Identify the blood parasite species.
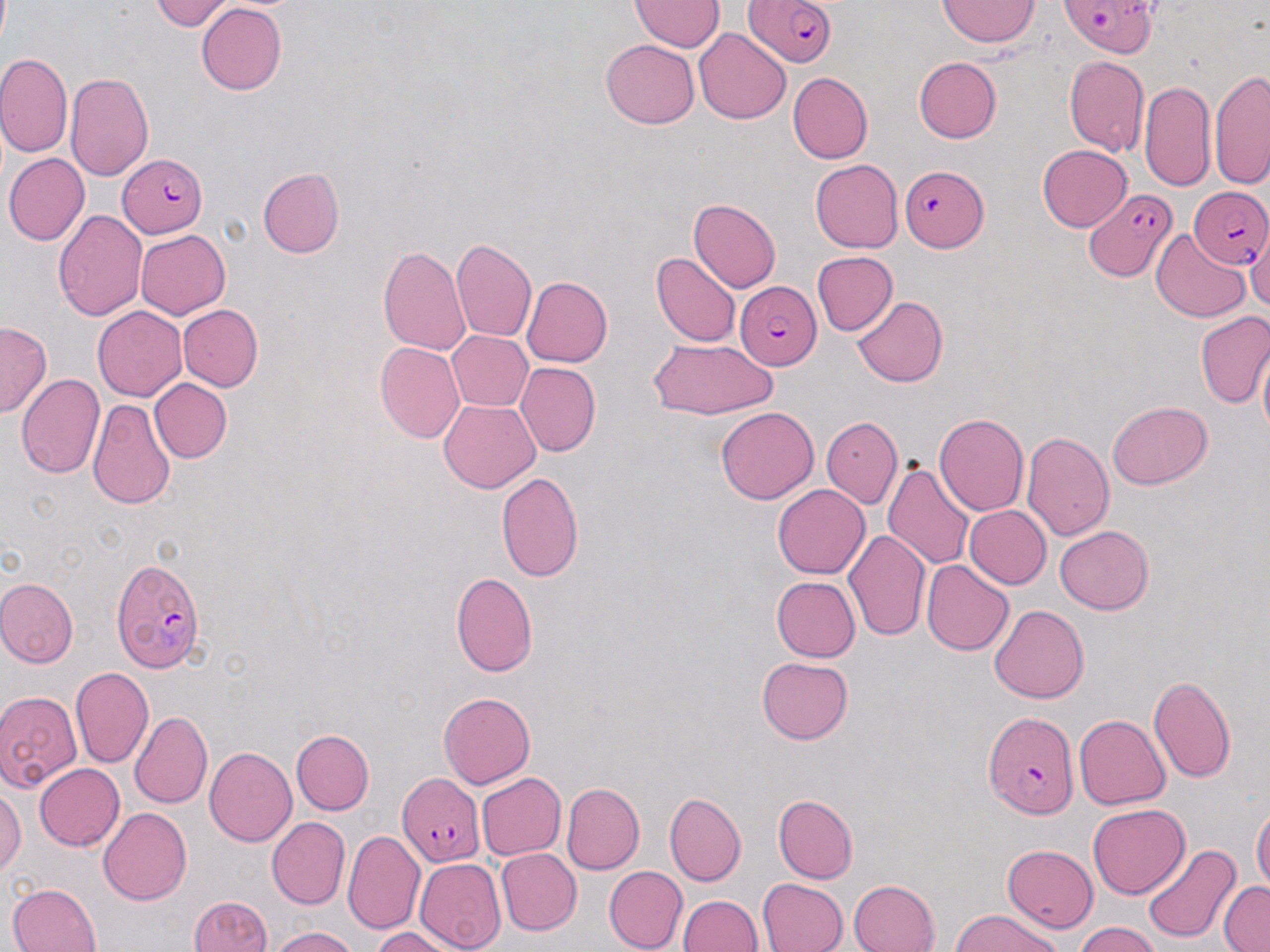
Plasmodium falciparum.

stain = May-Grünwald-Giemsa
field of view = single
modality = optical microscopy
magnification = 1000x
image size = 1270×952 pixels
preparation = thin blood film
uninfected red blood cell locations = approximate bounding boxes as (x1, y1, x2, y2) in pixels: (151, 0, 238, 31), (938, 0, 1041, 47), (631, 1, 723, 51), (196, 2, 286, 95), (693, 28, 791, 124), (600, 39, 700, 129), (0, 54, 72, 158), (1064, 54, 1149, 157), (913, 57, 1001, 144), (1210, 67, 1270, 191), (65, 72, 154, 180), (788, 72, 873, 163), (1139, 79, 1215, 194), (1038, 144, 1131, 231), (3, 153, 89, 246), (810, 159, 903, 252), (14, 162, 121, 279), (256, 168, 345, 258), (689, 199, 780, 292), (52, 208, 147, 320), (1246, 224, 1269, 313), (1151, 228, 1250, 322), (136, 230, 231, 319), (450, 237, 537, 341), (378, 245, 471, 354), (651, 251, 740, 347), (811, 251, 898, 336), (521, 276, 613, 367), (852, 296, 948, 387), (178, 303, 263, 391), (93, 306, 186, 400), (1194, 310, 1270, 409), (1, 320, 51, 418), (447, 330, 532, 411), (648, 337, 778, 419), (375, 342, 465, 443), (1257, 343, 1270, 443), (516, 362, 601, 456), (15, 374, 105, 478), (149, 378, 232, 463), (440, 399, 540, 492), (87, 400, 176, 510), (1107, 400, 1212, 489), (716, 406, 819, 504), (934, 414, 1029, 516), (821, 417, 902, 508), (1021, 431, 1115, 541), (882, 461, 975, 571), (495, 472, 584, 582), (772, 484, 870, 578), (963, 505, 1051, 588), (1054, 525, 1154, 613), (844, 529, 931, 641), (921, 558, 1015, 655), (451, 572, 538, 676), (770, 576, 860, 663), (0, 577, 78, 668), (990, 604, 1089, 704), (756, 657, 854, 745), (70, 666, 154, 768), (1148, 675, 1236, 783), (0, 690, 83, 790), (438, 691, 536, 788), (129, 711, 212, 808), (1074, 714, 1170, 809), (290, 730, 374, 815), (204, 747, 297, 847), (35, 763, 125, 851), (476, 772, 565, 860), (561, 781, 645, 875), (0, 787, 24, 876), (664, 792, 745, 886), (772, 793, 858, 883), (1087, 804, 1189, 899), (1252, 804, 1270, 894), (99, 807, 192, 905), (266, 817, 350, 909), (342, 829, 425, 934), (1142, 844, 1242, 944), (1003, 845, 1098, 932), (496, 848, 581, 936), (415, 858, 505, 952), (604, 865, 687, 952), (758, 877, 848, 952), (850, 879, 940, 952), (1218, 881, 1270, 951), (8, 882, 101, 951), (187, 895, 272, 952), (678, 895, 763, 952), (952, 910, 1065, 952), (1073, 921, 1161, 952), (267, 926, 361, 951), (371, 927, 463, 952)
Plasmodium falciparum-infected red blood cell locations = approximate bounding boxes as (x1, y1, x2, y2) in pixels: (744, 0, 840, 70), (1059, 1, 1160, 58), (118, 153, 209, 239), (900, 164, 988, 252), (1187, 186, 1269, 268), (1086, 189, 1176, 281), (735, 281, 822, 371), (111, 559, 207, 672), (983, 710, 1076, 819), (396, 772, 482, 863)